Report the malaria status of this cell.
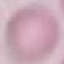

Uninfected.

Thin blood film. Giemsa stain. Cell patch, automatically extracted from a larger field of view and resized to 64 × 64 pixels. Photographed with a smartphone camera at the microscope eyepiece.